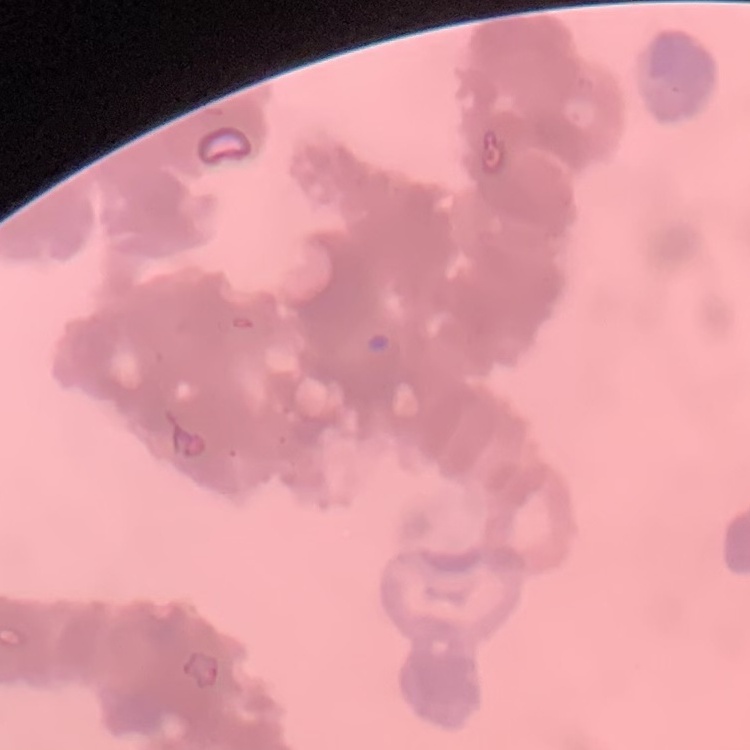 The red blood cells exhibit rouleaux formation. Thin blood film. Stained with either Field's or Giemsa. One tile cut from a larger photomicrograph.